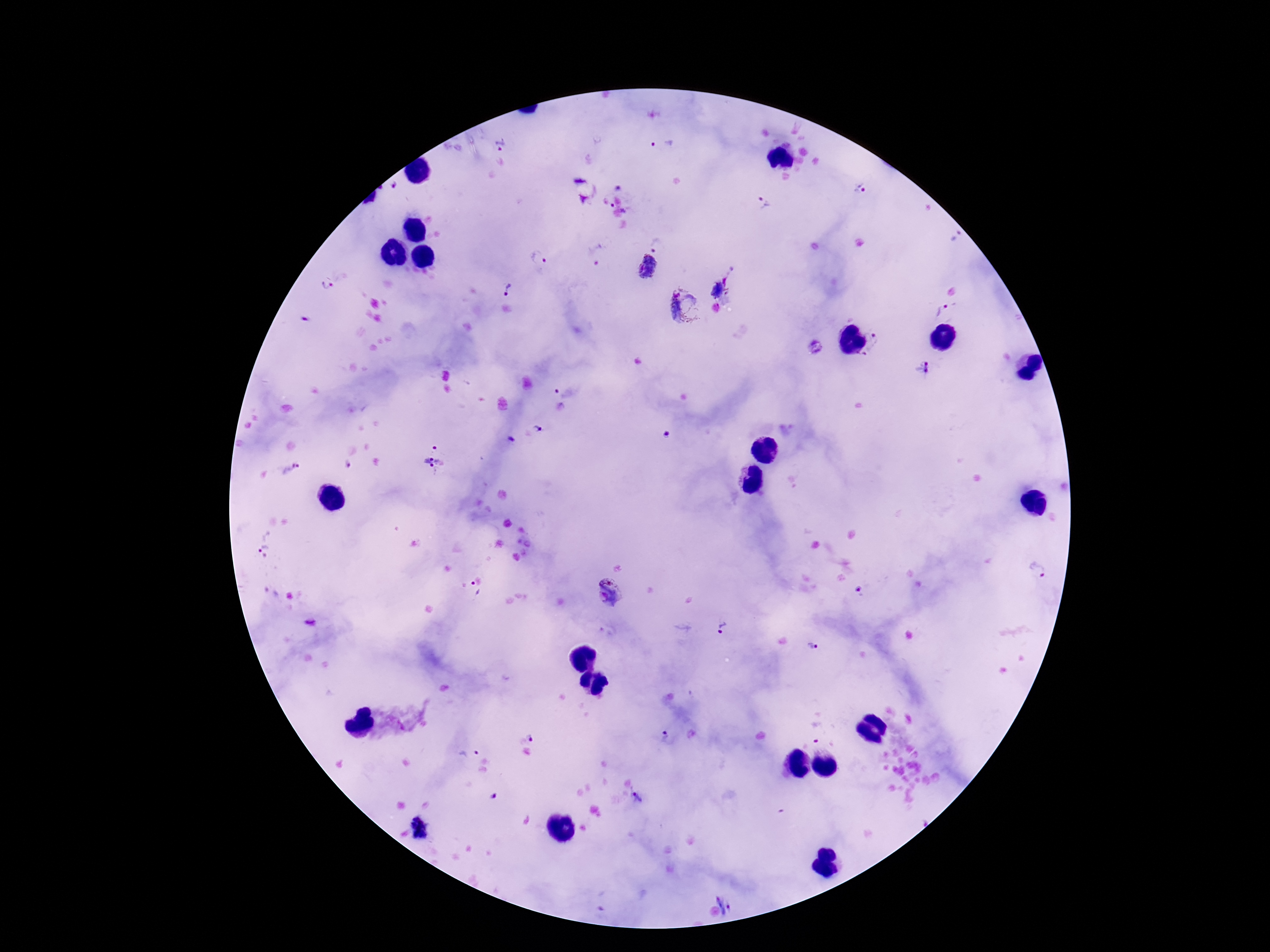
Approximate centers as [x, y] in pixels.
Summary:
  - Plasmodium parasite locations: [661, 144], [503, 145], [583, 189], [860, 189], [622, 194], [763, 204], [956, 236], [661, 240], [595, 255], [537, 259], [646, 268], [326, 287], [509, 289], [684, 308], [942, 312], [304, 320], [875, 343], [813, 347], [922, 368], [568, 387], [537, 429], [666, 436], [435, 457], [347, 467], [289, 470], [263, 546], [1037, 570], [860, 590], [472, 591], [610, 594], [310, 622], [721, 628], [814, 647], [816, 731], [525, 734], [668, 740], [467, 750], [494, 797], [639, 798], [420, 829], [732, 901]
  - Patient malaria status: infected
  - Image size: 1270×952 pixels
  - Capture: smartphone camera through the microscope eyepiece
  - Field of view: single
  - Preparation: thick peripheral-blood smear
  - Magnification: 100x
  - Stain: Giemsa